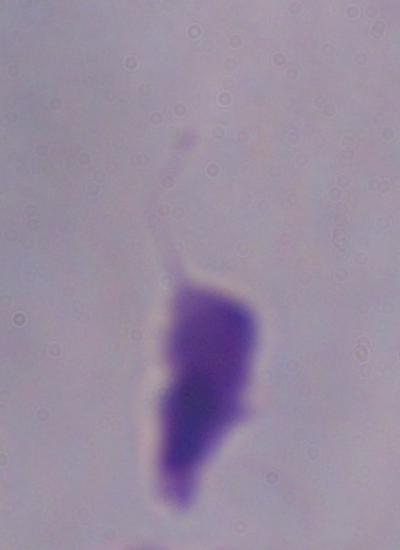
modality = photomicrograph
identification = trichomonad
magnification = 1000x